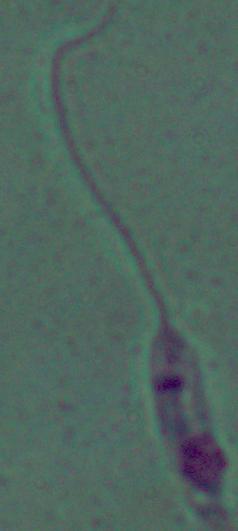

Summary:
  - Magnification: 1000x
  - Identification: Leishmania
  - Modality: photomicrograph